Identify the blood parasite species.
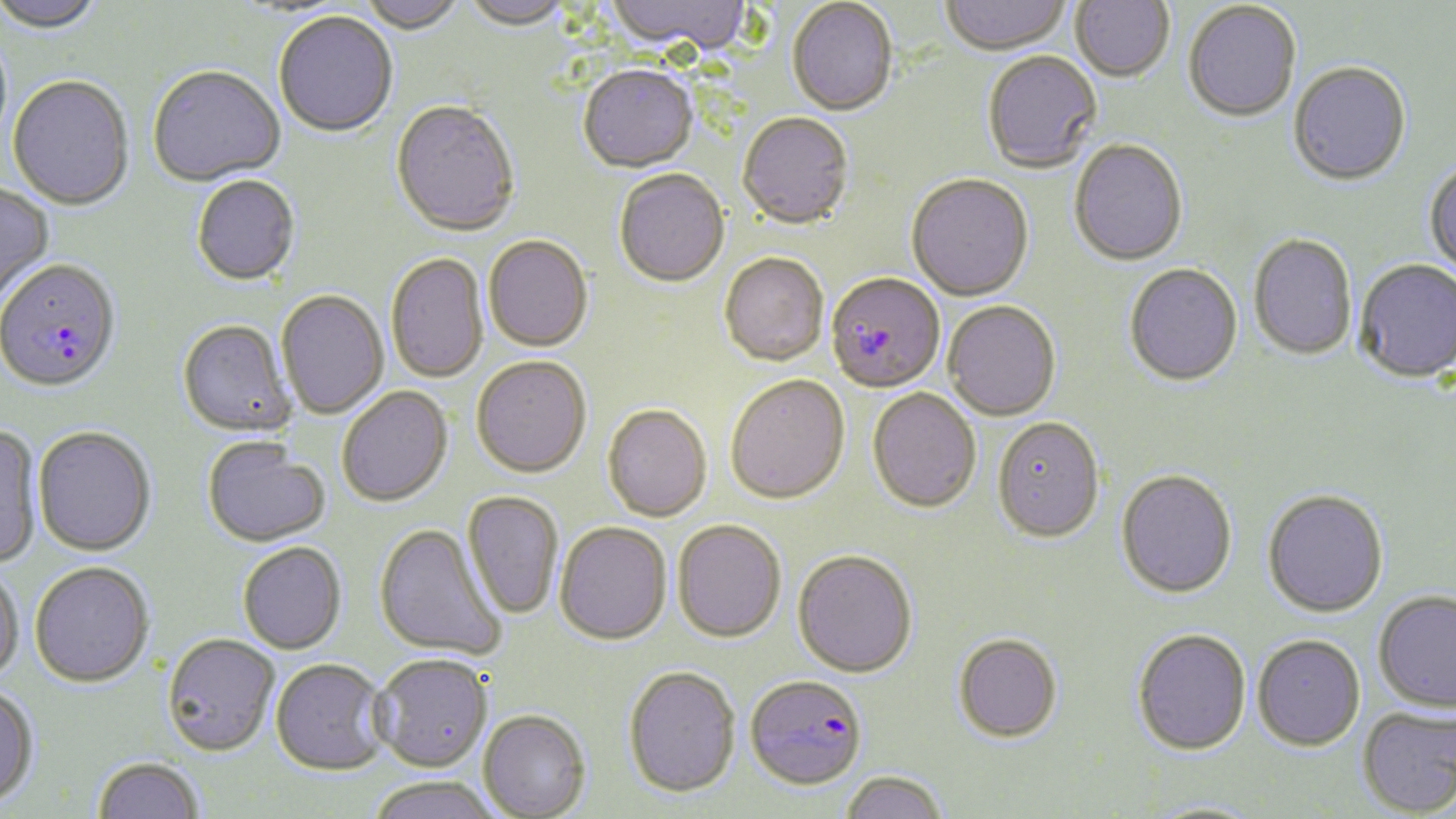
Plasmodium falciparum.

Summary:
  - Coordinate format: approximate bounding boxes as (x1,y1)-(x2,y2) corner pairs in pixels
  - Uninfected red blood cell locations: (1,0)-(105,36), (356,0)-(467,36), (462,0)-(572,34), (606,0)-(753,58), (941,0)-(1072,57), (1070,0)-(1174,84), (786,1)-(898,118), (1183,3)-(1302,125), (274,13)-(397,140), (983,53)-(1102,174), (1288,63)-(1411,188), (578,67)-(699,175), (148,68)-(286,190), (7,77)-(135,212), (390,102)-(520,240), (737,115)-(854,232), (1068,141)-(1188,268), (1424,159)-(1456,279), (614,171)-(729,290), (906,176)-(1034,303), (192,177)-(300,288), (0,183)-(54,306), (1248,235)-(1357,362), (483,237)-(593,354), (386,254)-(489,385), (720,255)-(829,368), (1354,260)-(1456,383), (1124,265)-(1243,388), (276,291)-(389,421), (943,303)-(1061,422), (177,321)-(296,439), (471,358)-(592,480), (726,377)-(850,506), (337,387)-(453,509), (867,389)-(981,515), (602,407)-(713,524), (992,420)-(1104,546), (0,423)-(44,569), (33,427)-(156,556), (202,438)-(330,548), (1115,471)-(1237,599), (1262,489)-(1388,617), (462,491)-(564,620), (672,522)-(786,645), (373,523)-(507,662), (555,524)-(672,648), (238,542)-(348,655), (792,552)-(918,680), (30,561)-(155,687), (0,565)-(24,684), (1373,589)-(1456,712), (1132,630)-(1251,757), (162,634)-(280,756), (953,634)-(1063,745), (1252,634)-(1366,751), (371,655)-(493,774), (270,659)-(390,776), (623,668)-(740,801), (0,685)-(40,807), (1357,705)-(1456,816), (479,711)-(591,819), (92,756)-(205,819), (840,771)-(949,819), (365,778)-(503,819), (1143,800)-(1270,818)
  - Plasmodium falciparum-infected red blood cell locations: (0,261)-(121,394), (826,275)-(946,396), (745,676)-(866,793)
  - Magnification: 1000x
  - Preparation: thin blood smear
  - Field of view: single
  - Modality: optical microscopy
  - Stain: May-Grünwald-Giemsa
  - Image size: 1456×819 pixels